Assess the morphology of the erythrocytes.
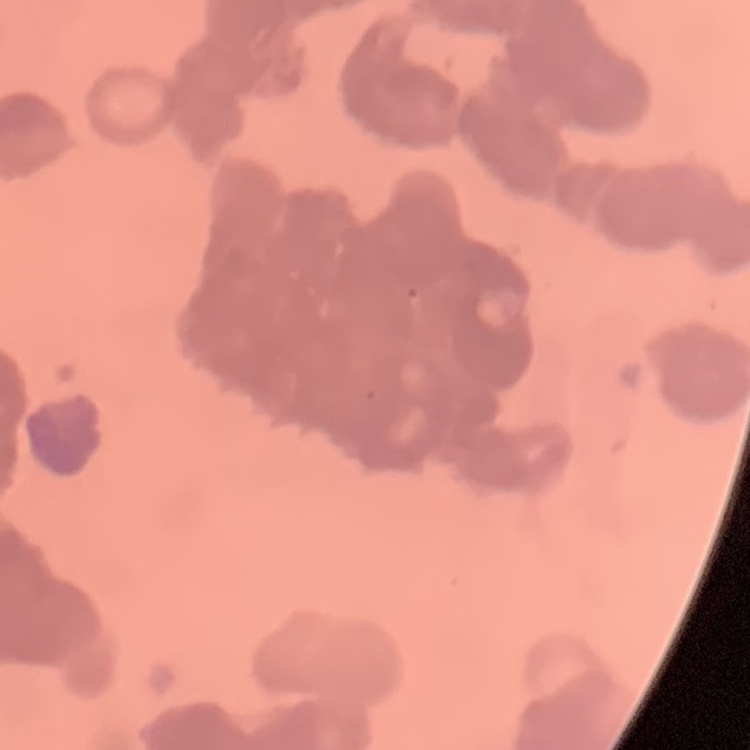

Rouleaux formation.

image_type: square crop of a larger photomicrograph
stain: Field's or Giemsa
preparation: thin peripheral smear